Report the malaria status of this cell.
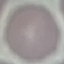

It is uninfected.

Summary:
  - Image type: cell patch, automatically extracted from a larger field of view and resized to 64 × 64 pixels
  - Stain: Giemsa
  - Preparation: thin smear
  - Capture: smartphone through the microscope eyepiece